Assess this cell for malaria.
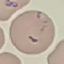

Parasitized.

preparation: thin blood smear
image_type: cell patch, automatically extracted from a larger field of view and resized to 64 × 64 pixels
capture: smartphone camera at the microscope eyepiece
stain: Giemsa